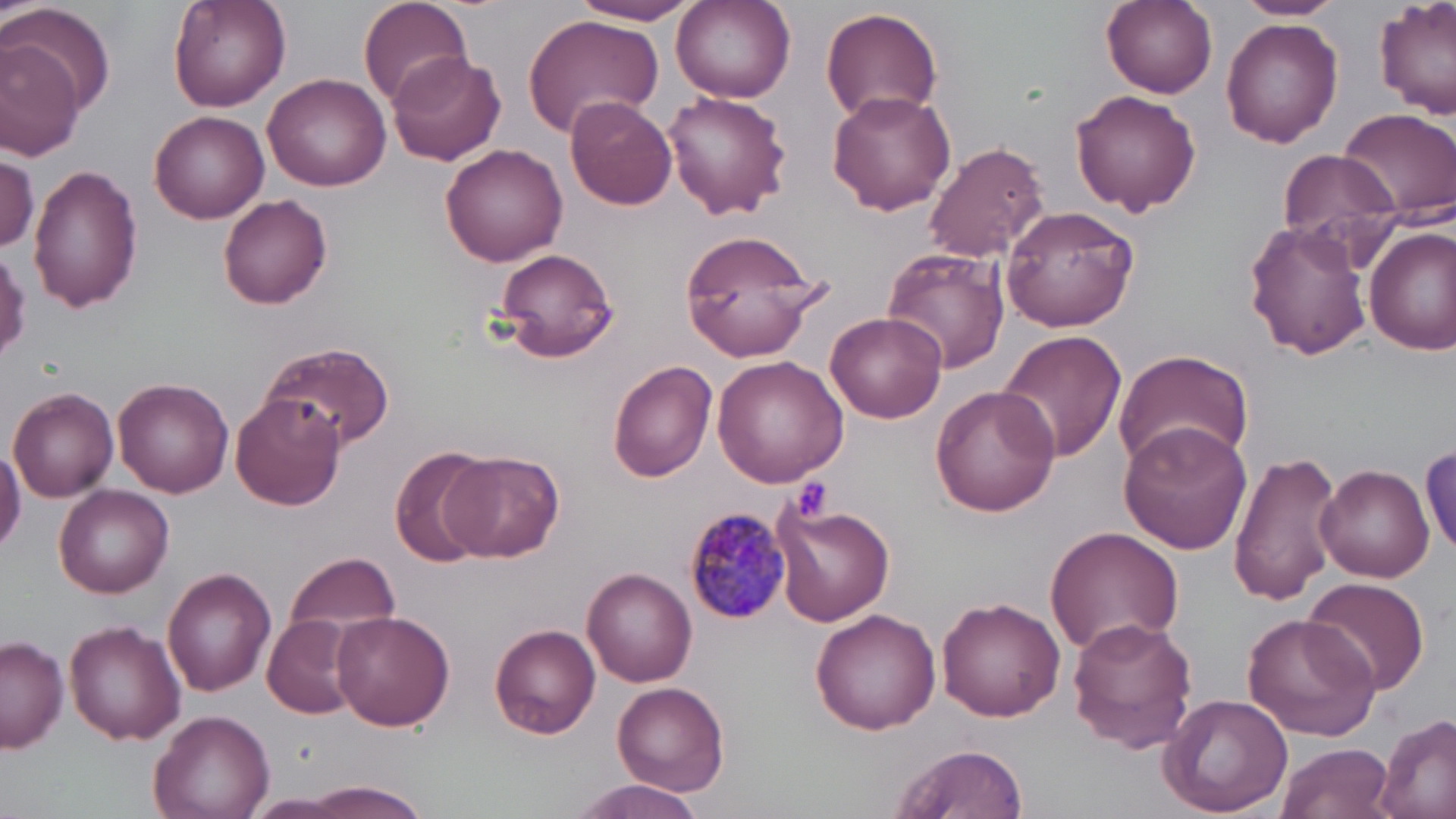

slide_level_diagnosis: Plasmodium malariae
uninfected_red_blood_cell_locations: 'approximate bounding boxes as named x1/y1/x2/y2 corners in pixels: (x1=165, y1=0, x2=290, y2=110), (x1=357, y1=0, x2=473, y2=109), (x1=570, y1=0, x2=701, y2=25), (x1=1101, y1=0, x2=1218, y2=98), (x1=1230, y1=0, x2=1348, y2=21), (x1=1375, y1=0, x2=1455, y2=119), (x1=5, y1=1, x2=117, y2=118), (x1=670, y1=1, x2=796, y2=105), (x1=819, y1=8, x2=945, y2=126), (x1=521, y1=10, x2=666, y2=141), (x1=1220, y1=18, x2=1343, y2=148), (x1=0, y1=33, x2=85, y2=159), (x1=385, y1=50, x2=507, y2=167), (x1=262, y1=71, x2=392, y2=191), (x1=1069, y1=89, x2=1203, y2=216), (x1=826, y1=90, x2=956, y2=214), (x1=661, y1=91, x2=792, y2=220), (x1=564, y1=98, x2=677, y2=211), (x1=1339, y1=107, x2=1456, y2=222), (x1=151, y1=110, x2=269, y2=224), (x1=922, y1=139, x2=1051, y2=262), (x1=441, y1=140, x2=568, y2=267), (x1=1278, y1=148, x2=1399, y2=254), (x1=1, y1=151, x2=39, y2=254), (x1=27, y1=166, x2=143, y2=311), (x1=218, y1=194, x2=333, y2=309), (x1=1001, y1=205, x2=1139, y2=332), (x1=1244, y1=219, x2=1372, y2=361), (x1=1365, y1=227, x2=1456, y2=356), (x1=679, y1=229, x2=833, y2=359), (x1=491, y1=246, x2=620, y2=364), (x1=880, y1=248, x2=1010, y2=375), (x1=825, y1=311, x2=947, y2=424), (x1=996, y1=330, x2=1129, y2=465), (x1=261, y1=340, x2=395, y2=451), (x1=1113, y1=348, x2=1255, y2=477), (x1=712, y1=355, x2=847, y2=488), (x1=606, y1=359, x2=717, y2=481), (x1=116, y1=379, x2=233, y2=496), (x1=8, y1=385, x2=118, y2=501), (x1=929, y1=386, x2=1059, y2=518), (x1=232, y1=394, x2=346, y2=511), (x1=1118, y1=422, x2=1251, y2=554), (x1=0, y1=440, x2=26, y2=556), (x1=1422, y1=443, x2=1456, y2=554), (x1=1226, y1=446, x2=1345, y2=606), (x1=390, y1=447, x2=495, y2=567), (x1=441, y1=450, x2=564, y2=561), (x1=1315, y1=463, x2=1434, y2=583), (x1=54, y1=485, x2=174, y2=598), (x1=772, y1=503, x2=892, y2=627), (x1=1044, y1=526, x2=1185, y2=653), (x1=283, y1=552, x2=400, y2=646), (x1=163, y1=567, x2=277, y2=697), (x1=582, y1=568, x2=698, y2=686), (x1=1299, y1=578, x2=1427, y2=697), (x1=938, y1=597, x2=1065, y2=723), (x1=811, y1=608, x2=943, y2=735), (x1=331, y1=610, x2=456, y2=732), (x1=1243, y1=613, x2=1383, y2=742), (x1=262, y1=615, x2=359, y2=719), (x1=1066, y1=616, x2=1199, y2=754), (x1=64, y1=620, x2=185, y2=745), (x1=490, y1=623, x2=603, y2=739), (x1=0, y1=634, x2=69, y2=753), (x1=612, y1=682, x2=731, y2=796), (x1=1158, y1=693, x2=1294, y2=816), (x1=149, y1=708, x2=275, y2=819), (x1=1374, y1=713, x2=1456, y2=819), (x1=887, y1=742, x2=1029, y2=819), (x1=1275, y1=743, x2=1396, y2=819), (x1=567, y1=776, x2=710, y2=819), (x1=293, y1=780, x2=431, y2=817)'
stain: May-Grünwald-Giemsa
platelet_locations: 'approximate bounding boxes as named x1/y1/x2/y2 corners in pixels: (x1=792, y1=477, x2=833, y2=521)'
image_size: 1456×819 pixels
field_of_view: single
plasmodium_malariae_infected_red_blood_cell_locations: 'approximate bounding boxes as named x1/y1/x2/y2 corners in pixels: (x1=683, y1=505, x2=793, y2=625)'
preparation: thin blood film
magnification: 1000x
modality: optical microscopy